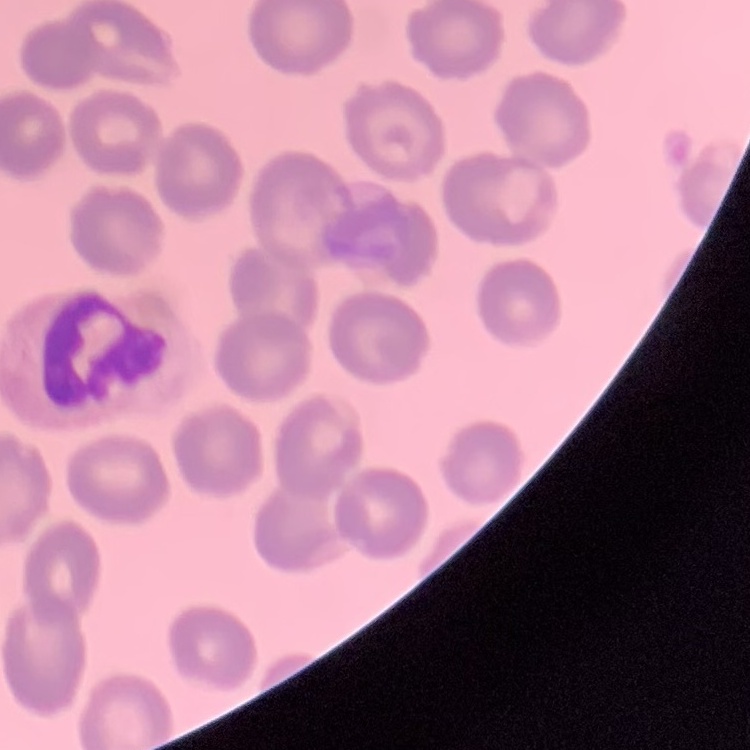

The red blood cells exhibit no rouleaux formation. Thin peripheral smear. Stained with either Field's or Giemsa. One tile cut from a larger photomicrograph.